Locate and identify every blood parasite.
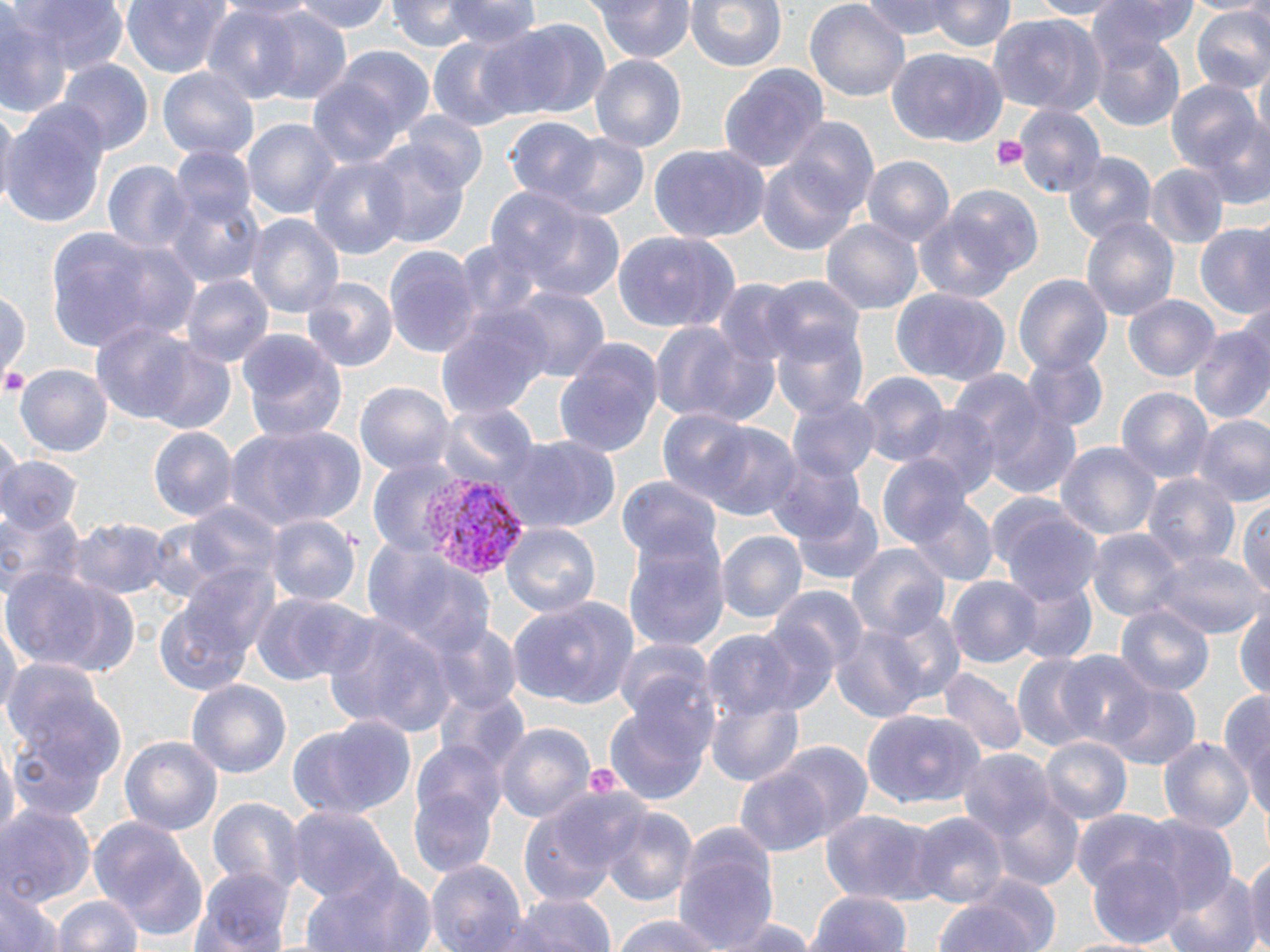

Approximate bounding boxes as (x1,y1)-(x2,y2) corner pairs in pixels.
Plasmodium vivax-infected red blood cells: (415,473)-(530,576).
No Plasmodium falciparum, Plasmodium ovale, Plasmodium malariae, Babesia divergens, or Trypanosoma brucei observed.

Summary:
  - Platelet locations: (990,134)-(1030,172), (581,762)-(625,802)
  - Uninfected red blood cell locations: (7,0)-(127,76), (122,0)-(229,81), (292,0)-(394,32), (387,0)-(487,51), (434,0)-(543,57), (594,0)-(693,63), (686,0)-(787,76), (804,0)-(912,104), (862,0)-(965,42), (931,0)-(1013,55), (1016,0)-(1129,20), (1089,0)-(1203,54), (1188,0)-(1270,17), (201,6)-(304,104), (247,7)-(357,109), (1188,7)-(1270,97), (985,12)-(1103,116), (1,15)-(73,119), (488,20)-(610,120), (1088,32)-(1186,131), (427,37)-(524,131), (326,45)-(434,143), (887,49)-(1006,149), (590,54)-(686,155), (60,60)-(150,155), (1253,61)-(1269,145), (720,63)-(827,174), (158,67)-(260,164), (305,74)-(408,170), (1166,80)-(1263,183), (0,101)-(111,231), (1,102)-(19,209), (1014,106)-(1104,200), (401,112)-(488,194), (1191,115)-(1270,210), (243,117)-(341,224), (504,117)-(603,210), (783,119)-(880,222), (546,133)-(652,224), (366,141)-(473,250), (647,141)-(771,244), (169,142)-(258,240), (1061,149)-(1155,245), (758,152)-(865,260), (308,156)-(409,259), (863,157)-(955,249), (102,161)-(191,257), (1144,164)-(1228,249), (163,177)-(266,291), (936,187)-(1042,282), (485,188)-(587,283), (503,199)-(628,304), (916,213)-(1018,303), (247,214)-(344,324), (1081,215)-(1179,323), (820,220)-(922,316), (45,226)-(197,354), (1195,226)-(1270,322), (611,231)-(743,333), (384,245)-(482,355), (1014,272)-(1111,377), (181,275)-(275,370), (762,275)-(862,362), (303,278)-(400,372), (710,278)-(805,370), (889,287)-(1011,387), (506,288)-(609,385), (0,290)-(31,382), (1122,293)-(1222,383), (436,307)-(541,428), (770,319)-(870,420), (87,321)-(210,429), (646,321)-(763,427), (1189,323)-(1270,428), (237,329)-(348,441), (138,338)-(240,432), (552,338)-(664,458), (1023,351)-(1110,436), (16,363)-(112,458), (856,373)-(951,465), (968,376)-(1085,503), (354,379)-(455,478), (1115,386)-(1213,487), (786,394)-(880,485), (906,406)-(999,498), (658,408)-(761,505), (1192,413)-(1270,509), (222,423)-(366,534), (699,423)-(804,523), (147,425)-(240,524), (502,436)-(620,536), (1055,443)-(1159,542), (0,450)-(78,533), (766,455)-(866,549), (878,455)-(977,554), (1142,474)-(1238,571), (618,476)-(721,569), (791,494)-(884,585), (990,497)-(1103,606), (906,498)-(999,586), (178,501)-(282,598), (1240,502)-(1270,598), (0,506)-(81,609), (266,514)-(360,607), (70,515)-(169,601), (501,522)-(600,621), (1087,528)-(1184,624), (717,531)-(806,626), (623,537)-(729,655), (366,541)-(495,662), (846,542)-(949,642), (1158,548)-(1264,642), (159,566)-(277,694), (5,567)-(141,675), (946,575)-(1043,669), (1013,576)-(1097,665), (773,588)-(870,677), (507,593)-(640,710), (251,594)-(364,689), (1233,598)-(1270,704), (1115,601)-(1214,699), (868,606)-(971,709), (321,614)-(454,739), (0,616)-(20,727), (436,625)-(524,715), (832,626)-(930,725), (701,629)-(811,721), (611,638)-(712,721), (1056,649)-(1156,751), (1010,655)-(1105,755), (1,659)-(126,814), (938,667)-(1025,759), (186,681)-(292,778), (1105,681)-(1200,771), (1222,684)-(1270,822), (436,690)-(532,783), (707,697)-(804,785), (605,700)-(711,807), (862,709)-(985,810), (290,714)-(418,821), (493,720)-(596,826), (119,734)-(223,837), (1158,734)-(1256,836), (1040,737)-(1130,827), (412,739)-(507,838), (2,740)-(20,844), (774,742)-(871,840), (959,748)-(1058,849), (733,771)-(832,855), (407,786)-(499,880), (982,789)-(1084,890), (207,797)-(302,895), (518,800)-(629,906), (1,803)-(95,908), (599,805)-(697,903), (286,806)-(395,902), (1072,809)-(1176,897), (906,810)-(1009,909), (818,811)-(937,900), (89,814)-(211,944), (1134,818)-(1238,914), (672,821)-(780,952), (1245,848)-(1270,952), (1087,852)-(1187,948), (424,859)-(528,952), (301,865)-(439,952), (191,867)-(295,951), (1164,870)-(1259,952), (0,881)-(58,952), (495,891)-(618,952), (807,892)-(911,952), (51,894)-(145,952), (928,896)-(1049,952), (611,914)-(734,952), (716,916)-(816,952), (1051,934)-(1159,951)
  - Slide-level diagnosis: Plasmodium vivax
  - Magnification: 1000x
  - Field of view: one of a larger specimen
  - Stain: May-Grünwald-Giemsa
  - Preparation: thin blood film
  - Modality: optical microscopy
  - Image size: 1270×952 pixels